Assess the morphology of the erythrocytes.
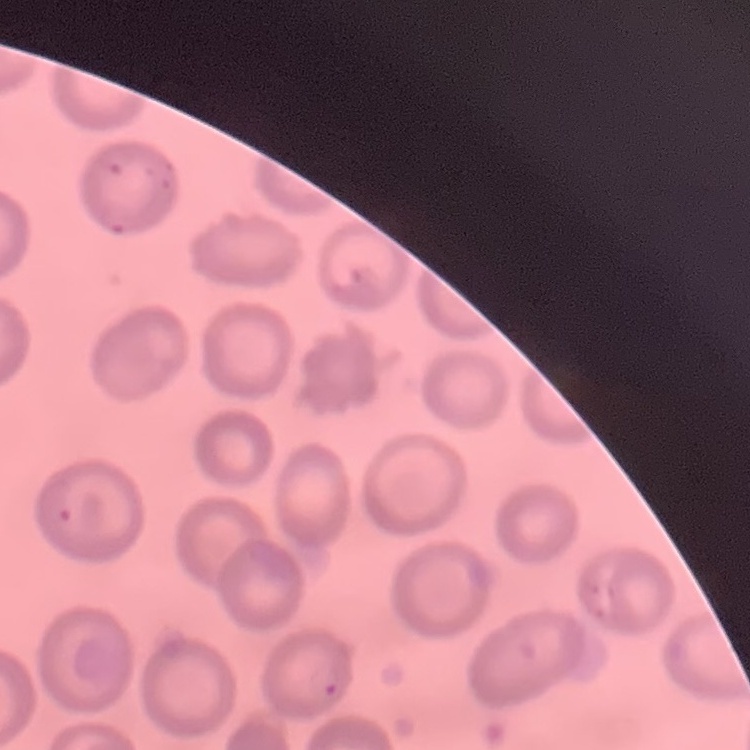
They show no rouleaux formation.

Summary:
  - Image type: square crop of a larger photomicrograph
  - Preparation: thin peripheral smear
  - Stain: Field's or Giemsa